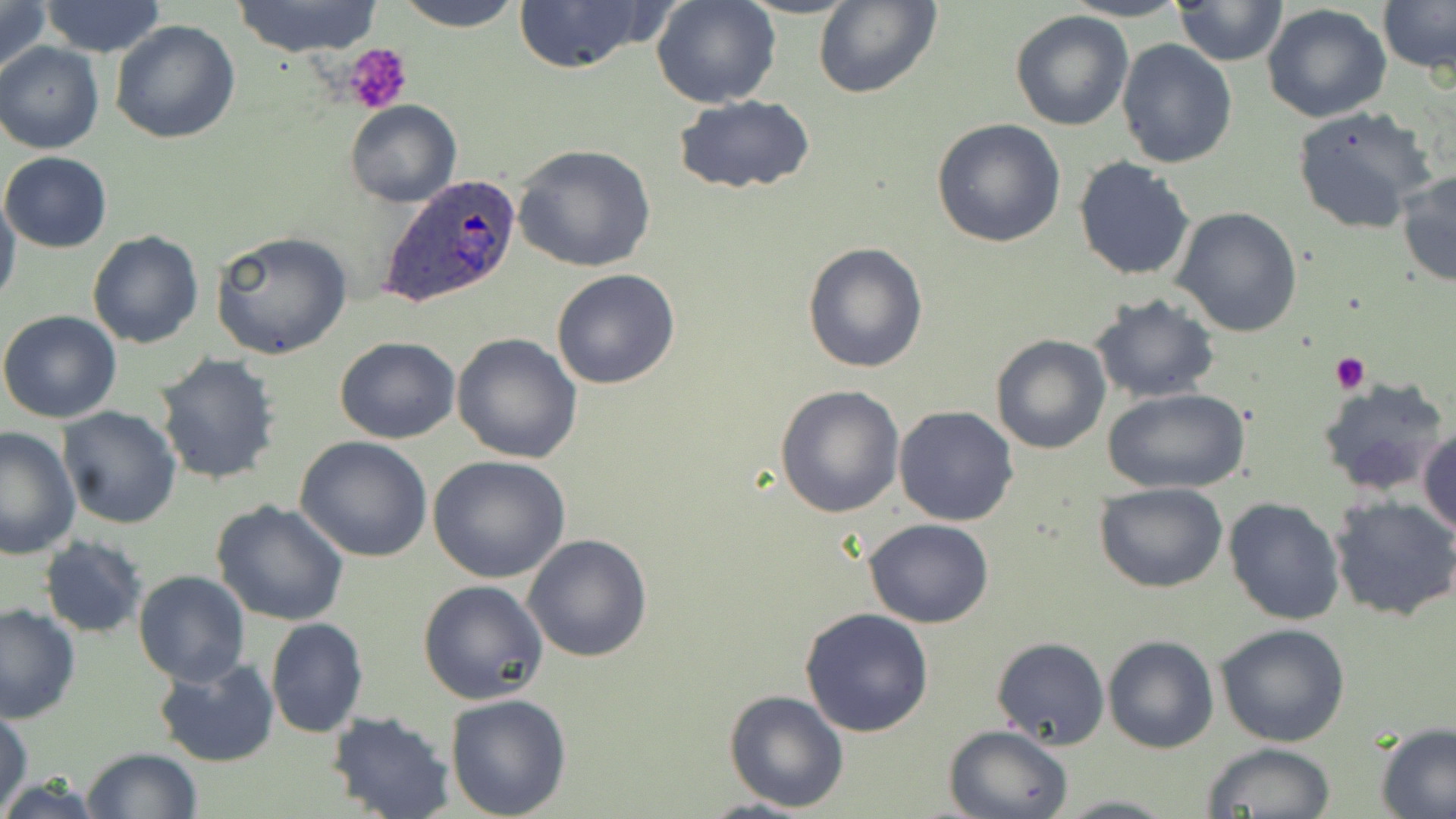 Approximate bounding boxes as [x1, y1, x2, y2] in pixels. Uninfected red blood cell locations: [0, 0, 51, 83], [37, 0, 168, 57], [387, 0, 529, 30], [650, 0, 782, 108], [813, 0, 943, 100], [1061, 0, 1191, 22], [1379, 0, 1455, 74], [234, 1, 383, 54], [509, 1, 658, 74], [1172, 1, 1287, 65], [1262, 3, 1393, 124], [1010, 10, 1134, 131], [109, 19, 241, 144], [1116, 40, 1238, 170], [0, 41, 104, 154], [674, 96, 818, 196], [344, 100, 461, 207], [1291, 105, 1438, 237], [931, 118, 1066, 249], [511, 143, 658, 272], [1, 150, 111, 251], [1073, 157, 1197, 281], [1397, 169, 1456, 288], [0, 190, 21, 308], [1171, 206, 1303, 337], [87, 230, 203, 349], [209, 230, 353, 360], [801, 243, 928, 373], [550, 269, 680, 390], [1088, 293, 1222, 404], [0, 309, 122, 423], [451, 333, 583, 464], [989, 334, 1112, 455], [333, 336, 461, 444], [154, 353, 281, 487], [1317, 377, 1449, 499], [774, 384, 906, 518], [1105, 387, 1249, 495], [894, 406, 1019, 527], [57, 407, 183, 530], [1418, 425, 1456, 540], [0, 426, 81, 560], [294, 436, 434, 562], [427, 454, 570, 582], [1095, 482, 1228, 593], [1224, 496, 1345, 625], [1330, 496, 1456, 622], [212, 499, 349, 627], [864, 518, 994, 629], [522, 533, 655, 663], [38, 537, 147, 638], [132, 570, 251, 687], [418, 579, 548, 704], [0, 603, 80, 724], [799, 607, 935, 737], [265, 618, 368, 738], [1214, 624, 1352, 748], [1102, 635, 1218, 754], [991, 636, 1109, 752], [151, 657, 279, 768], [723, 688, 851, 813], [443, 693, 572, 818], [0, 705, 33, 814], [325, 711, 456, 819], [1374, 723, 1456, 818], [942, 724, 1072, 818], [1200, 743, 1337, 818], [81, 747, 202, 819], [1052, 794, 1181, 819]. Platelet locations: [342, 46, 411, 115], [1331, 352, 1370, 394]. Plasmodium ovale-infected red blood cell locations: [379, 173, 523, 310]. Slide-level diagnosis: Plasmodium ovale. One field of a larger specimen. Optical microscopy. Captured at 1000x magnification. Image is 1456×819 pixels. Thin blood smear. May-Grünwald-Giemsa stain.